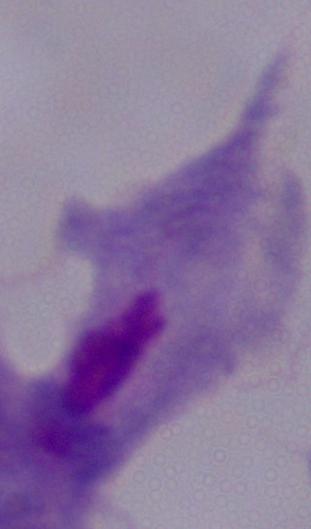

Summary:
  - Magnification: 1000x
  - Identification: trichomonad
  - Modality: micrograph